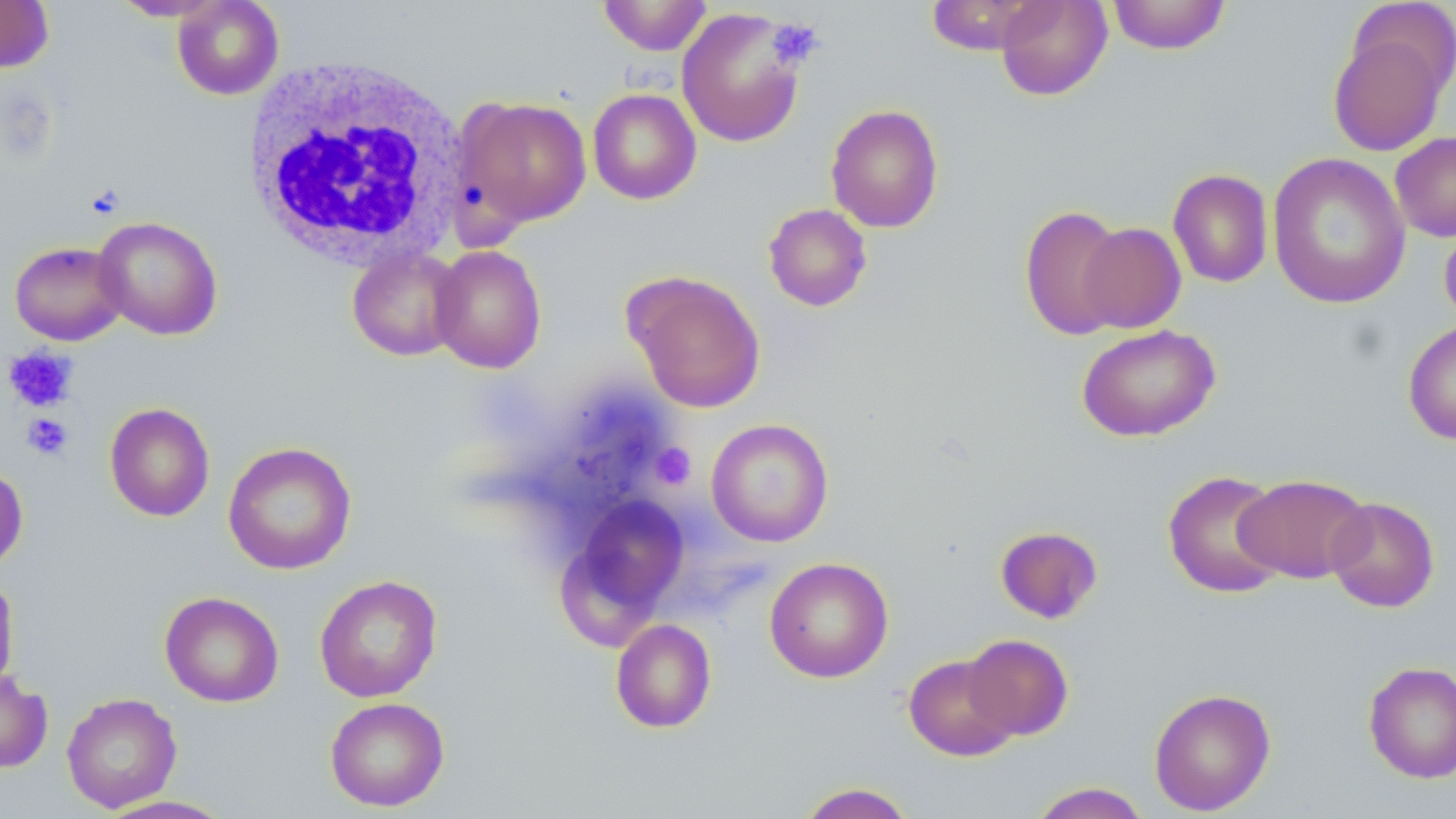
slide-level diagnosis = negative for blood parasites
modality = light microscopy
field of view = single
platelet locations = approximate bounding boxes as (x1,y1)-(x2,y2) corner pairs in pixels: (767,19)-(823,68), (3,345)-(79,412), (21,413)-(73,460), (651,443)-(696,489)
image size = 1456×819 pixels
white blood cell locations = approximate bounding boxes as (x1,y1)-(x2,y2) corner pairs in pixels: (241,54)-(470,270)
preparation = thin blood film
magnification = 1000x
uninfected red blood cell locations = approximate bounding boxes as (x1,y1)-(x2,y2) corner pairs in pixels: (0,0)-(54,73), (109,0)-(229,21), (171,0)-(285,100), (597,0)-(713,55), (926,0)-(1047,55), (995,0)-(1112,101), (1106,0)-(1232,55), (1345,2)-(1456,101), (676,8)-(807,148), (1328,28)-(1450,157), (587,88)-(702,205), (454,97)-(592,230), (825,103)-(944,233), (1390,131)-(1456,242), (1267,152)-(1411,310), (1168,169)-(1274,288), (763,203)-(872,311), (1019,204)-(1128,341), (93,216)-(223,341), (1439,219)-(1456,329), (1078,222)-(1186,333), (9,241)-(127,345), (429,244)-(547,373), (347,246)-(465,361), (624,270)-(766,413), (1403,320)-(1456,445), (1076,324)-(1220,442), (104,402)-(215,522), (706,418)-(834,547), (222,441)-(358,575), (0,463)-(28,571), (1162,470)-(1287,599), (1235,474)-(1371,583), (561,493)-(690,635), (1325,496)-(1439,612), (994,525)-(1103,624), (764,557)-(894,683), (0,571)-(20,698), (314,574)-(443,702), (159,591)-(284,707), (610,618)-(717,733), (963,634)-(1074,741), (903,653)-(1020,761), (1363,661)-(1456,784), (0,668)-(53,773), (1149,687)-(1276,815), (61,692)-(182,812), (324,696)-(450,812), (795,782)-(918,819), (1028,782)-(1152,819), (94,795)-(237,819)
stain = May-Grünwald-Giemsa